Classify this cell by malaria status.
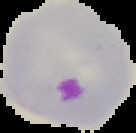

Parasitized.

Summary:
  - Image type: segmented cell region with the area outside set to black
  - Image size: 136×133 pixels
  - Preparation: thin blood smear